Point out each Plasmodium parasite.
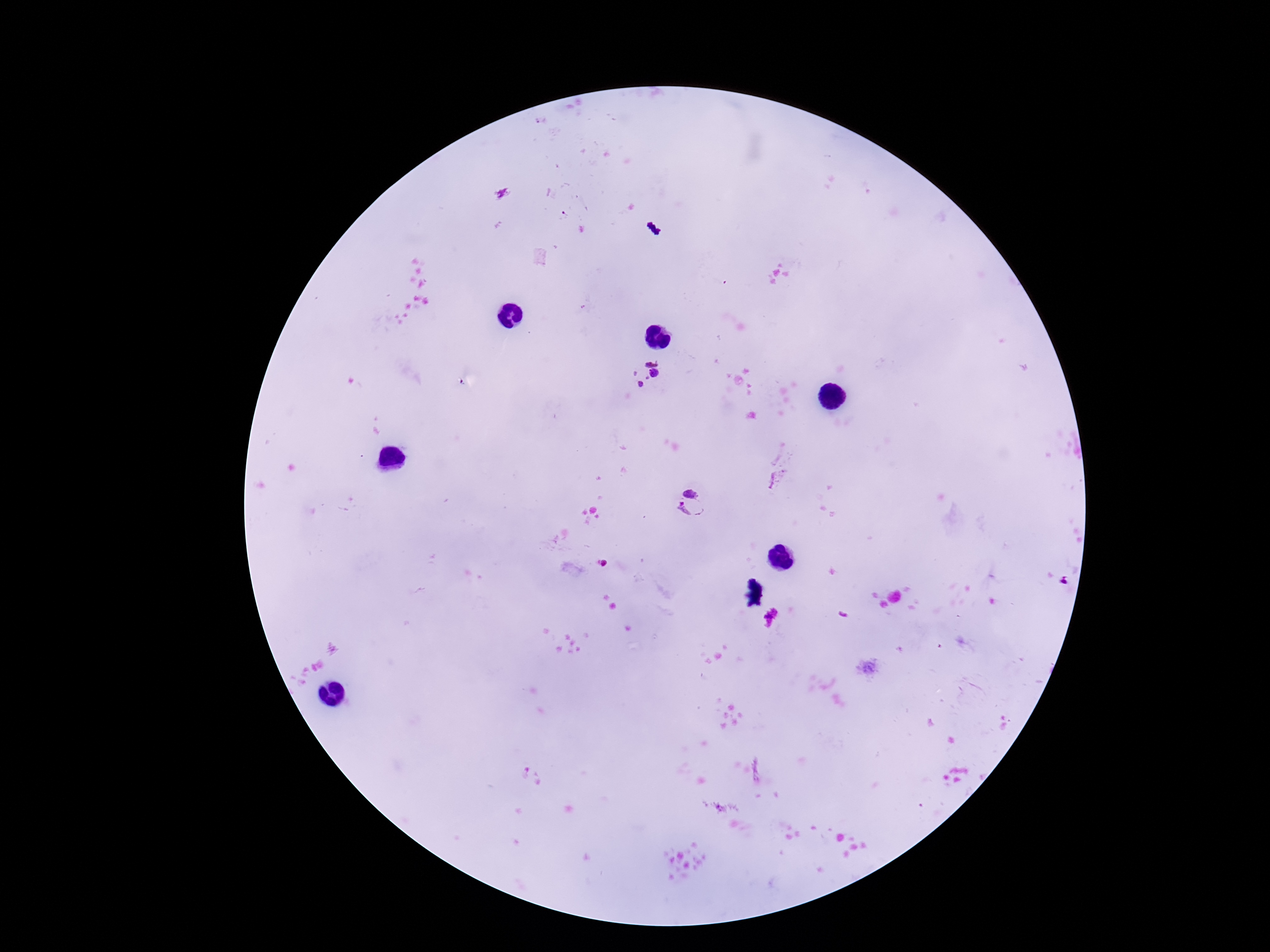

Approximate object centers, in pixels from the top-left corner.
Plasmodium parasites: (x=645, y=373), (x=691, y=504).

field of view = single
image size = 1270×952 pixels
preparation = thick peripheral-blood smear
magnification = 100x
patient malaria status = positive
capture = smartphone camera through the microscope eyepiece
stain = Giemsa